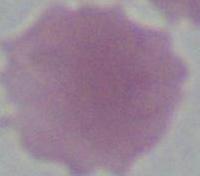
A red blood cell is seen. Micrograph. Captured at 1000x magnification.